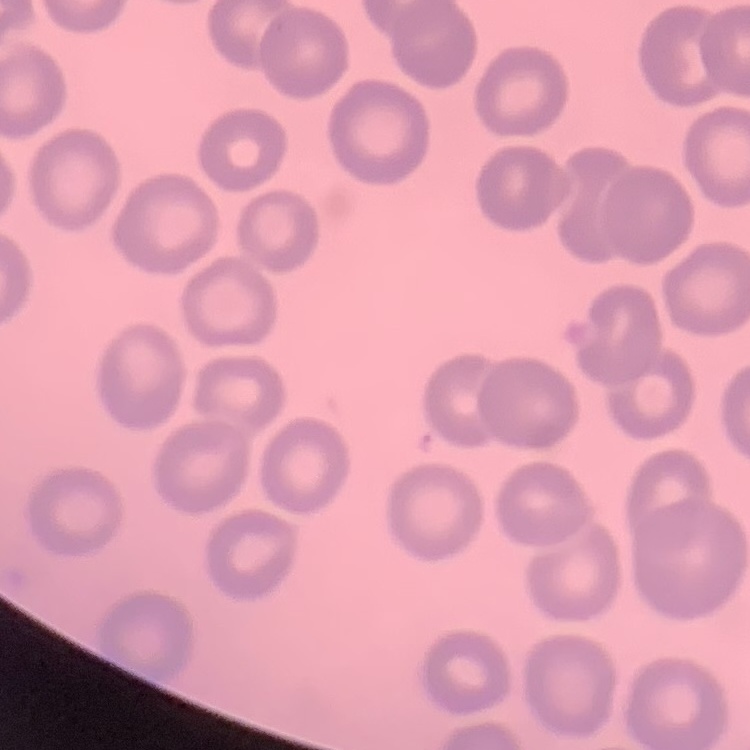

The erythrocytes show no rouleaux formation. Stained with either Field's or Giemsa. One tile cut from a larger photomicrograph. Thin blood film.